Assess the morphology of the erythrocytes.
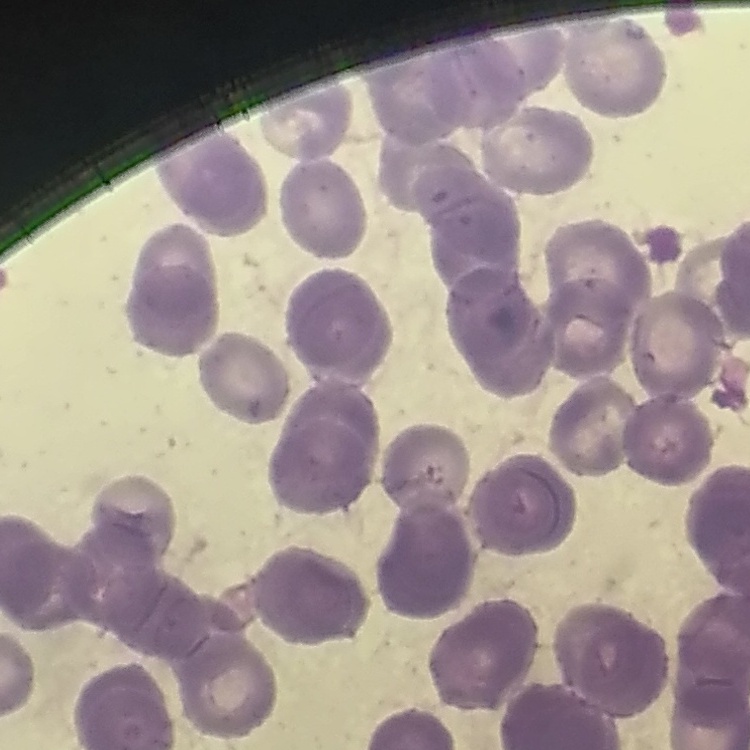

They show rouleaux formation.

Summary:
  - Preparation: thin blood film
  - Stain: Field's or Giemsa
  - Image type: one tile cut from a larger photomicrograph